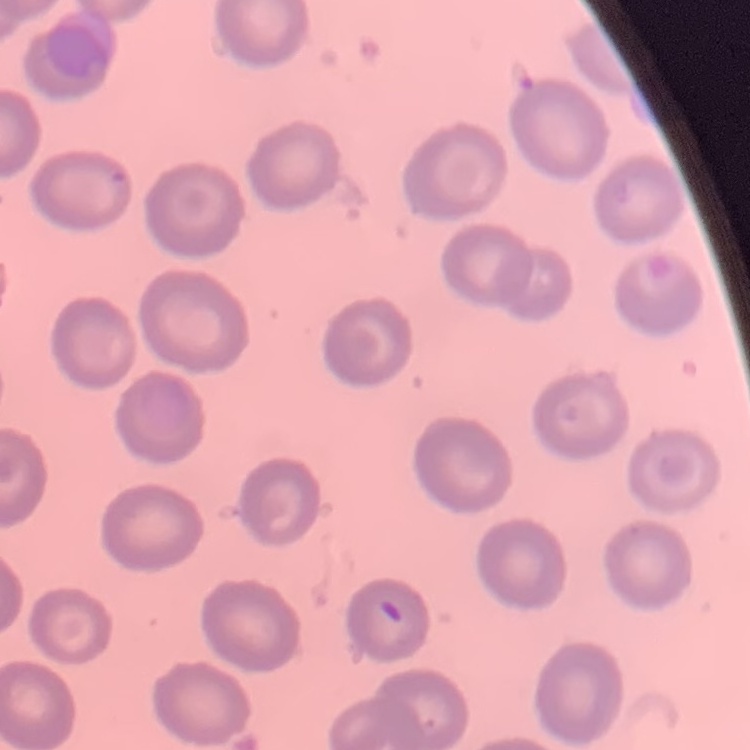
The red blood cells show no rouleaux formation. Field's or Giemsa stain. One tile cut from a larger photomicrograph. Thin blood smear.